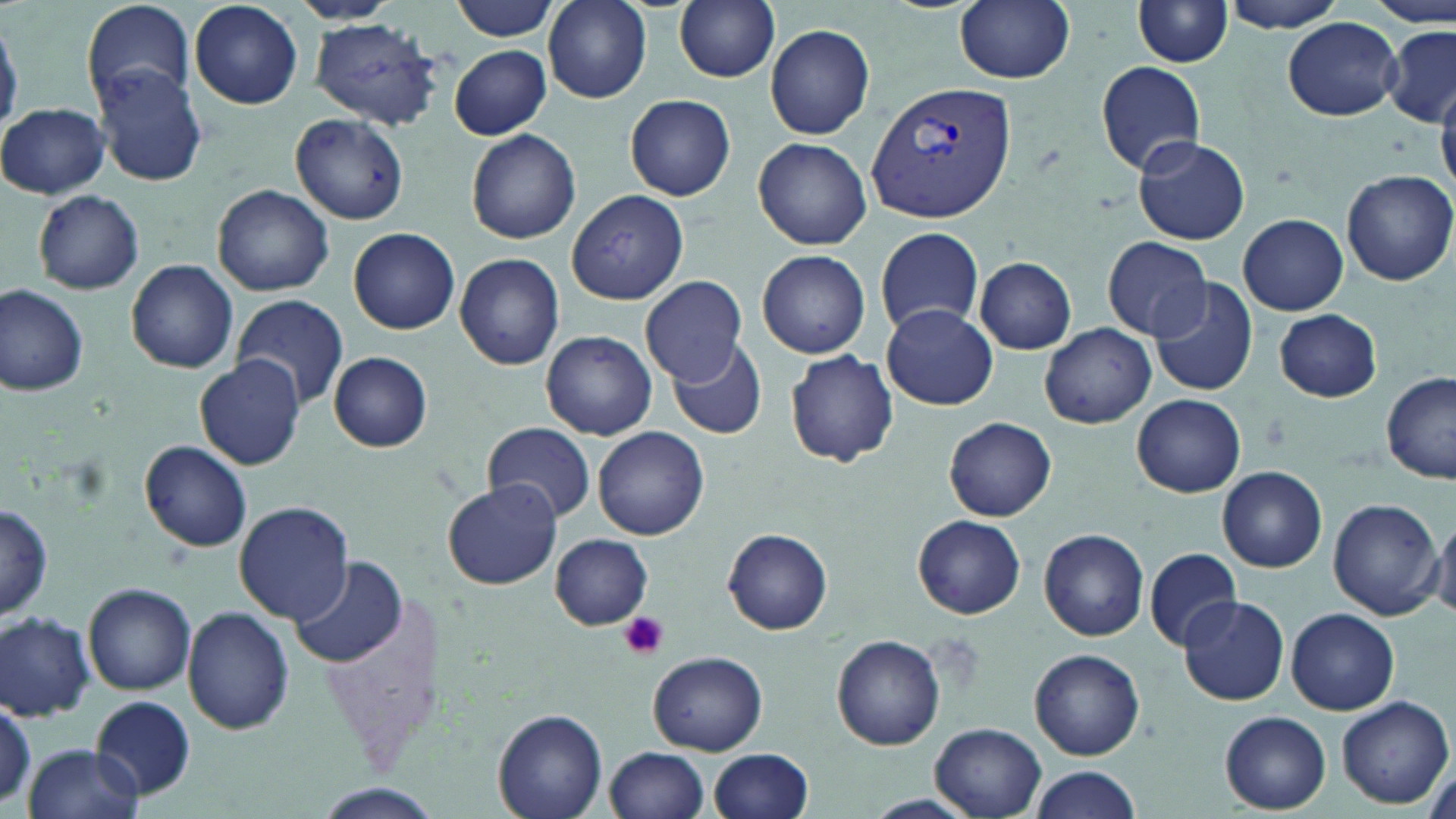

Summary:
  - Coordinate format: approximate bounding boxes as (x1, y1, x2, y2) in pixels
  - Platelet locations: (618, 611, 668, 660)
  - Uninfected red blood cell locations: (81, 0, 197, 109), (448, 0, 561, 41), (544, 0, 652, 103), (674, 0, 780, 83), (954, 0, 1076, 84), (1133, 0, 1232, 67), (1220, 0, 1350, 33), (1369, 0, 1451, 24), (291, 1, 402, 26), (190, 2, 303, 110), (310, 16, 443, 130), (1283, 17, 1402, 121), (766, 25, 875, 139), (1383, 25, 1456, 124), (449, 45, 553, 140), (1097, 61, 1206, 174), (92, 65, 210, 186), (1434, 71, 1456, 195), (624, 94, 736, 200), (0, 103, 111, 200), (290, 113, 410, 225), (465, 129, 582, 244), (1132, 136, 1250, 246), (753, 137, 872, 250), (1342, 170, 1455, 286), (212, 184, 334, 296), (33, 189, 145, 294), (565, 189, 689, 305), (1238, 214, 1348, 314), (875, 225, 985, 337), (348, 226, 460, 334), (1102, 236, 1211, 340), (756, 249, 871, 359), (454, 251, 566, 370), (973, 257, 1077, 353), (126, 258, 239, 374), (640, 274, 746, 383), (1147, 278, 1260, 399), (1, 283, 90, 395), (229, 294, 350, 408), (882, 305, 997, 410), (1275, 309, 1382, 401), (1039, 323, 1156, 429), (539, 330, 659, 440), (668, 336, 769, 440), (784, 349, 901, 466), (328, 351, 433, 452), (195, 357, 304, 470), (1382, 372, 1456, 483), (1132, 394, 1246, 497), (944, 417, 1056, 522), (482, 421, 594, 523), (593, 426, 709, 539), (139, 440, 252, 551), (1215, 466, 1328, 572), (442, 481, 561, 590), (1327, 497, 1444, 619), (233, 502, 356, 626), (1, 503, 54, 619), (913, 515, 1026, 618), (1431, 515, 1456, 620), (722, 528, 833, 634), (1038, 528, 1150, 642), (549, 534, 653, 629), (1143, 546, 1244, 651), (292, 555, 406, 668), (83, 582, 196, 694), (316, 585, 449, 773), (1178, 596, 1289, 706), (183, 607, 295, 735), (1286, 608, 1399, 714), (0, 610, 96, 719), (830, 634, 946, 751), (1029, 648, 1145, 761), (648, 651, 768, 755), (1336, 694, 1455, 808), (90, 697, 198, 798), (493, 709, 607, 819), (1221, 711, 1330, 814), (930, 723, 1047, 818), (22, 743, 143, 818), (605, 747, 711, 819), (708, 749, 814, 819), (1027, 767, 1140, 819), (309, 786, 443, 818), (868, 793, 975, 816)
  - Plasmodium vivax-infected red blood cell locations: (865, 82, 1016, 222)
  - Slide-level diagnosis: Plasmodium vivax
  - Preparation: thin blood smear
  - Modality: light microscopy
  - Field of view: single
  - Stain: May-Grünwald-Giemsa
  - Image size: 1456×819 pixels
  - Magnification: 1000x